Comment on the morphology of the red blood cells.
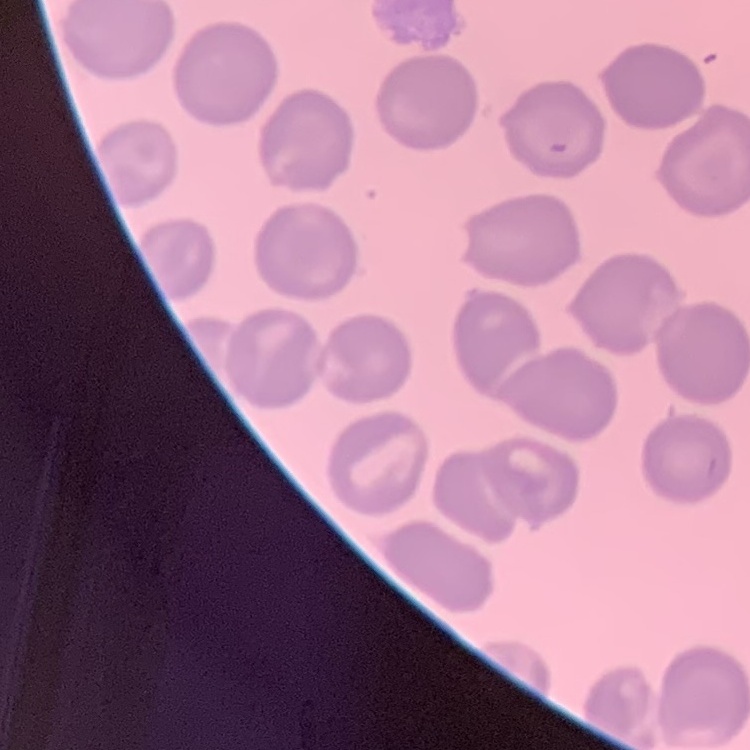
They show no rouleaux formation.

Summary:
  - Preparation: thin blood smear
  - Stain: Field's or Giemsa
  - Image type: one tile cut from a larger photomicrograph